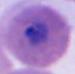
Summary:
  - Magnification: 400x or 1000x
  - Identification: Plasmodium
  - Modality: photomicrograph